Give the extent of all Plasmodium falciparum-infected red blood cells.
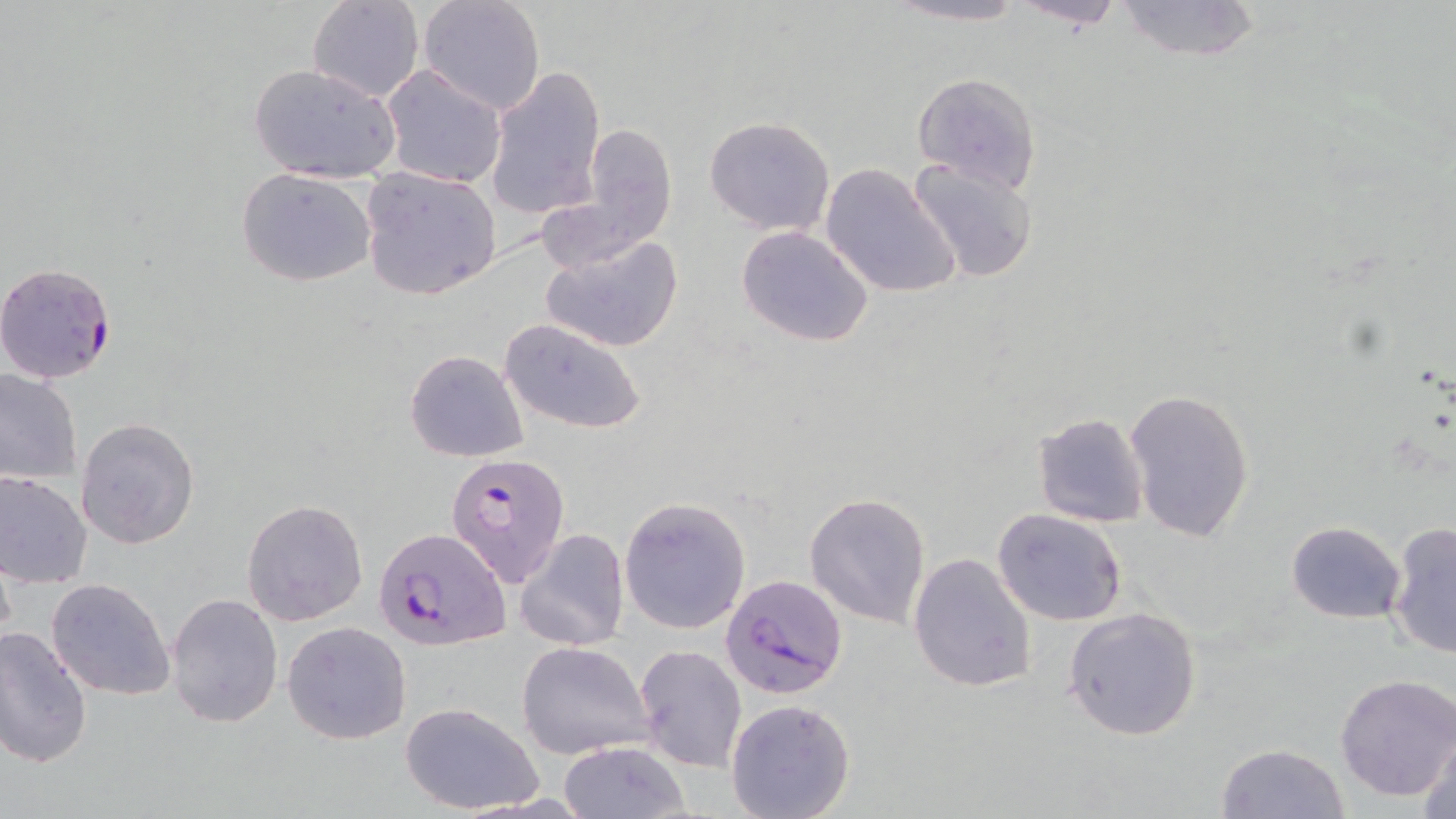

Approximate bounding boxes as named x1/y1/x2/y2 corners in pixels.
Plasmodium falciparum-infected red blood cells: (x1=1, y1=260, x2=110, y2=391), (x1=445, y1=454, x2=571, y2=588), (x1=375, y1=525, x2=510, y2=650), (x1=722, y1=574, x2=849, y2=700).

{
  "slide_level_diagnosis": "Plasmodium falciparum",
  "preparation": "thin blood film",
  "stain": "May-Grünwald-Giemsa",
  "magnification": "1000x",
  "image_size": "1456×819 pixels",
  "field_of_view": "single",
  "uninfected_red_blood_cell_locations": "approximate bounding boxes as named x1/y1/x2/y2 corners in pixels: (x1=307, y1=0, x2=423, y2=103), (x1=416, y1=0, x2=544, y2=115), (x1=1009, y1=0, x2=1130, y2=32), (x1=1112, y1=0, x2=1263, y2=63), (x1=880, y1=1, x2=1033, y2=27), (x1=248, y1=63, x2=402, y2=185), (x1=380, y1=65, x2=508, y2=188), (x1=484, y1=66, x2=606, y2=220), (x1=910, y1=72, x2=1041, y2=193), (x1=703, y1=116, x2=836, y2=236), (x1=579, y1=124, x2=677, y2=251), (x1=908, y1=157, x2=1038, y2=283), (x1=821, y1=162, x2=961, y2=299), (x1=358, y1=166, x2=502, y2=301), (x1=235, y1=167, x2=376, y2=285), (x1=736, y1=225, x2=875, y2=348), (x1=539, y1=234, x2=683, y2=354), (x1=498, y1=317, x2=647, y2=435), (x1=405, y1=349, x2=529, y2=461), (x1=0, y1=366, x2=82, y2=483), (x1=1124, y1=387, x2=1255, y2=545), (x1=1033, y1=413, x2=1149, y2=527), (x1=75, y1=416, x2=200, y2=551), (x1=0, y1=469, x2=93, y2=587), (x1=804, y1=492, x2=931, y2=629), (x1=618, y1=496, x2=751, y2=634), (x1=243, y1=498, x2=367, y2=626), (x1=992, y1=509, x2=1129, y2=626), (x1=1284, y1=520, x2=1405, y2=624), (x1=1386, y1=521, x2=1456, y2=660), (x1=515, y1=528, x2=629, y2=654), (x1=907, y1=552, x2=1037, y2=694), (x1=46, y1=578, x2=176, y2=701), (x1=166, y1=592, x2=284, y2=727), (x1=1062, y1=605, x2=1204, y2=741), (x1=283, y1=621, x2=412, y2=745), (x1=0, y1=626, x2=94, y2=768), (x1=516, y1=641, x2=655, y2=759), (x1=634, y1=643, x2=747, y2=773), (x1=1334, y1=672, x2=1456, y2=802), (x1=725, y1=699, x2=857, y2=819), (x1=401, y1=703, x2=543, y2=815), (x1=1419, y1=726, x2=1456, y2=818), (x1=558, y1=740, x2=691, y2=819), (x1=1214, y1=742, x2=1351, y2=818)",
  "modality": "light microscopy"
}